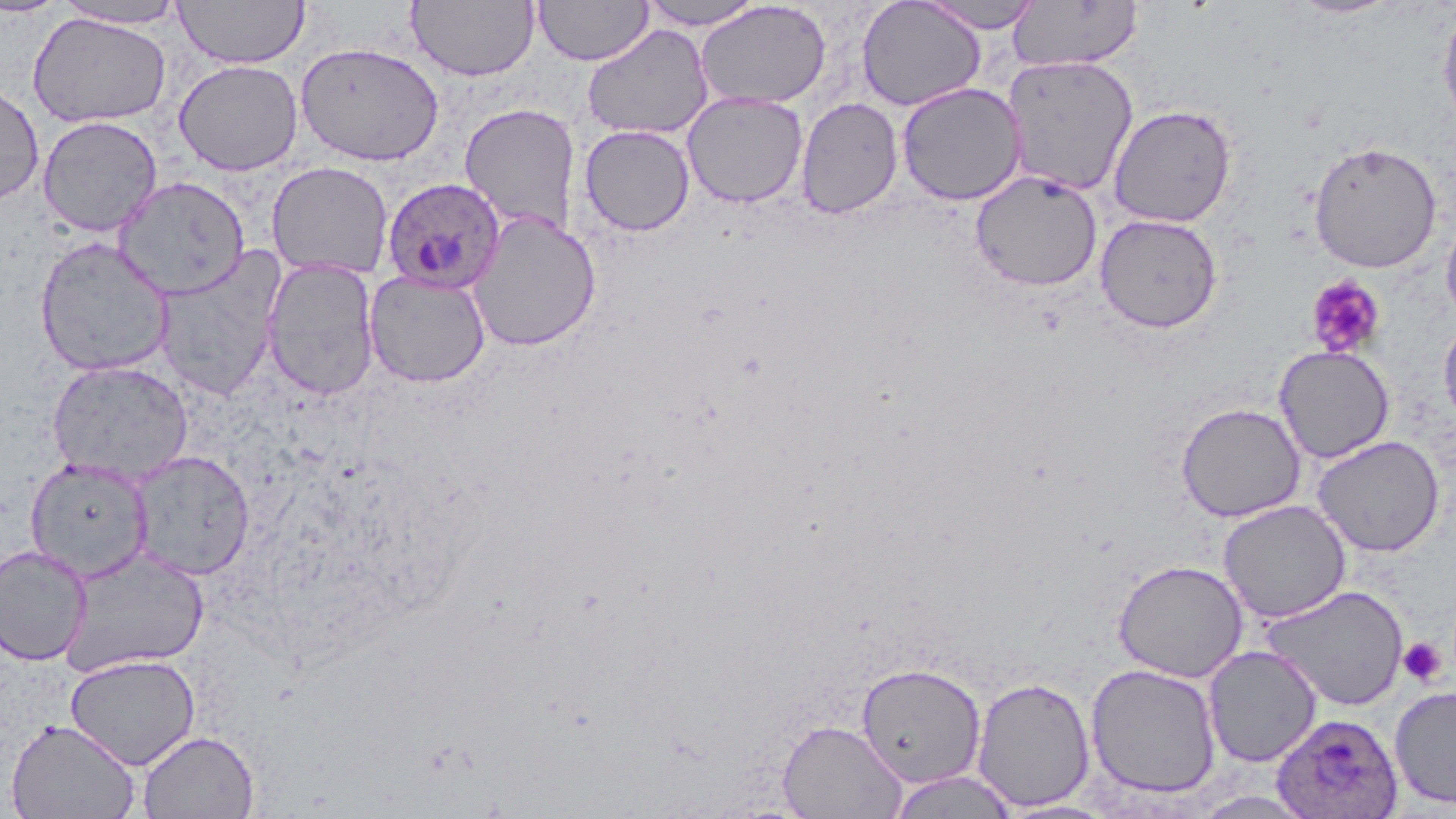

slide-level diagnosis = Plasmodium ovale
stain = May-Grünwald-Giemsa
modality = optical microscopy
platelet locations = approximate bounding boxes as (x1, y1, x2, y2) in pixels: (1305, 274, 1386, 358), (1397, 637, 1447, 687)
preparation = thin blood film
uninfected red blood cell locations = approximate bounding boxes as (x1, y1, x2, y2) in pixels: (0, 0, 67, 18), (174, 0, 307, 69), (407, 0, 539, 82), (534, 0, 653, 66), (641, 0, 764, 30), (856, 0, 987, 111), (1286, 0, 1403, 19), (53, 1, 189, 30), (694, 1, 831, 110), (918, 1, 1045, 33), (1007, 1, 1143, 73), (1437, 3, 1456, 134), (27, 12, 171, 128), (582, 24, 714, 140), (295, 41, 444, 167), (1002, 54, 1139, 196), (173, 59, 303, 176), (0, 81, 44, 205), (896, 82, 1027, 206), (682, 91, 808, 209), (795, 97, 903, 220), (459, 104, 580, 238), (1108, 104, 1236, 228), (37, 115, 163, 237), (579, 125, 695, 237), (1308, 141, 1442, 273), (266, 161, 393, 280), (970, 170, 1103, 291), (114, 176, 250, 299), (1441, 209, 1456, 328), (467, 210, 601, 352), (1095, 213, 1223, 334), (34, 236, 174, 378), (152, 249, 287, 402), (261, 258, 380, 400), (364, 270, 491, 388), (1438, 314, 1456, 435), (1274, 344, 1395, 463), (46, 360, 194, 484), (1176, 402, 1306, 522), (1312, 435, 1445, 557), (129, 450, 255, 580), (26, 458, 153, 582), (1218, 500, 1351, 624), (0, 545, 92, 665), (59, 547, 210, 678), (1112, 559, 1249, 682), (1259, 583, 1409, 712), (1203, 645, 1323, 767), (65, 654, 199, 770), (856, 662, 987, 788), (1085, 663, 1222, 800), (972, 676, 1096, 812), (1389, 684, 1456, 810), (5, 718, 140, 819), (777, 718, 908, 818), (137, 730, 259, 818), (885, 770, 1021, 818)
Plasmodium ovale-infected red blood cell locations = approximate bounding boxes as (x1, y1, x2, y2) in pixels: (381, 176, 507, 293), (1271, 712, 1404, 818)
image size = 1456×819 pixels
field of view = single
magnification = 1000x